Describe the morphology of the erythrocytes.
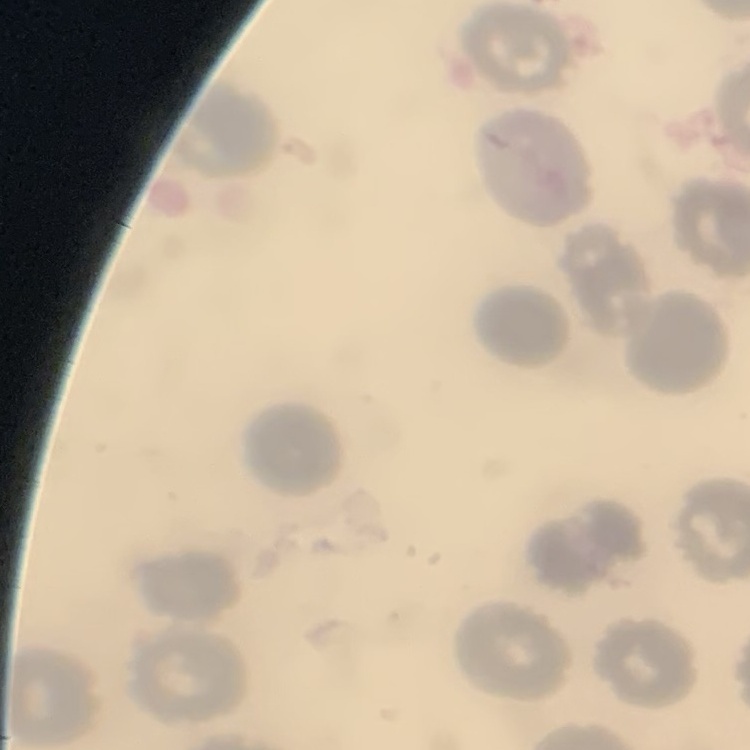
No rouleaux formation.

{
  "stain": "Field's or Giemsa",
  "image_type": "square crop of a larger photomicrograph",
  "preparation": "thin peripheral smear"
}